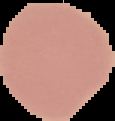
image size = 115×121 pixels
preparation = thin blood film
malaria status = uninfected
image type = cell region segmented out of the field of view; surrounding area masked to black